Identify the blood parasite species.
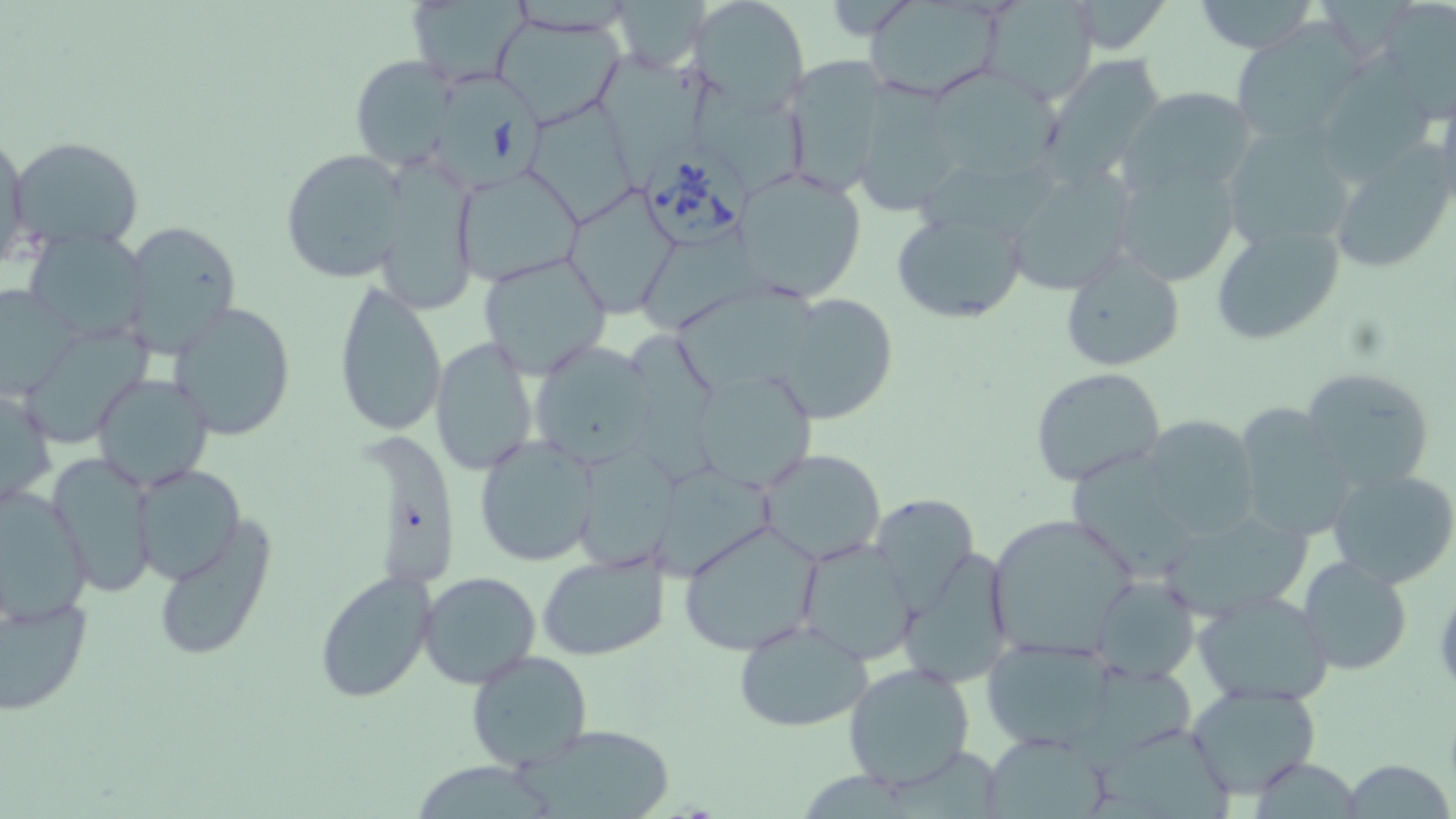

Babesia divergens.

Summary:
  - Coordinate format: approximate bounding boxes as named x1/y1/x2/y2 corners in pixels
  - Babesia divergens-infected red blood cell locations: (x1=435, y1=73, x2=552, y2=195), (x1=640, y1=151, x2=749, y2=247)
  - Uninfected red blood cell locations: (x1=612, y1=0, x2=708, y2=72), (x1=687, y1=0, x2=808, y2=114), (x1=980, y1=0, x2=1097, y2=106), (x1=1190, y1=0, x2=1322, y2=54), (x1=405, y1=1, x2=528, y2=85), (x1=861, y1=1, x2=1006, y2=100), (x1=1064, y1=2, x2=1174, y2=54), (x1=1376, y1=3, x2=1454, y2=115), (x1=493, y1=13, x2=625, y2=127), (x1=1231, y1=24, x2=1364, y2=149), (x1=588, y1=51, x2=716, y2=185), (x1=1040, y1=54, x2=1170, y2=179), (x1=350, y1=55, x2=467, y2=172), (x1=782, y1=56, x2=891, y2=194), (x1=928, y1=71, x2=1062, y2=180), (x1=693, y1=81, x2=818, y2=197), (x1=852, y1=84, x2=965, y2=216), (x1=1121, y1=86, x2=1257, y2=196), (x1=534, y1=104, x2=643, y2=228), (x1=1220, y1=124, x2=1360, y2=256), (x1=0, y1=134, x2=29, y2=268), (x1=8, y1=136, x2=146, y2=254), (x1=1327, y1=147, x2=1456, y2=275), (x1=282, y1=148, x2=410, y2=285), (x1=1110, y1=155, x2=1246, y2=287), (x1=371, y1=162, x2=481, y2=318), (x1=1004, y1=163, x2=1139, y2=296), (x1=453, y1=166, x2=585, y2=285), (x1=737, y1=167, x2=868, y2=302), (x1=562, y1=185, x2=682, y2=317), (x1=889, y1=207, x2=1029, y2=324), (x1=118, y1=218, x2=244, y2=358), (x1=1211, y1=218, x2=1347, y2=345), (x1=23, y1=229, x2=152, y2=343), (x1=1058, y1=248, x2=1186, y2=372), (x1=476, y1=252, x2=613, y2=377), (x1=332, y1=282, x2=448, y2=437), (x1=0, y1=285, x2=79, y2=399), (x1=770, y1=292, x2=899, y2=425), (x1=679, y1=293, x2=839, y2=400), (x1=169, y1=300, x2=297, y2=442), (x1=30, y1=317, x2=158, y2=440), (x1=429, y1=338, x2=538, y2=476), (x1=526, y1=339, x2=658, y2=468), (x1=1298, y1=364, x2=1436, y2=493), (x1=690, y1=366, x2=820, y2=493), (x1=1028, y1=366, x2=1167, y2=486), (x1=91, y1=372, x2=215, y2=491), (x1=0, y1=383, x2=55, y2=514), (x1=1231, y1=404, x2=1356, y2=542), (x1=1139, y1=414, x2=1261, y2=538), (x1=474, y1=435, x2=599, y2=566), (x1=757, y1=448, x2=888, y2=566), (x1=569, y1=449, x2=687, y2=576), (x1=48, y1=454, x2=158, y2=597), (x1=1068, y1=458, x2=1200, y2=576), (x1=133, y1=464, x2=246, y2=585), (x1=1326, y1=467, x2=1456, y2=589), (x1=651, y1=468, x2=782, y2=582), (x1=0, y1=485, x2=92, y2=626), (x1=870, y1=493, x2=978, y2=600), (x1=1155, y1=508, x2=1313, y2=622), (x1=989, y1=515, x2=1142, y2=658), (x1=153, y1=518, x2=275, y2=662), (x1=678, y1=520, x2=824, y2=658), (x1=794, y1=539, x2=920, y2=665), (x1=536, y1=548, x2=671, y2=662), (x1=898, y1=549, x2=1016, y2=687), (x1=1298, y1=556, x2=1412, y2=675), (x1=314, y1=570, x2=438, y2=701), (x1=419, y1=572, x2=542, y2=690), (x1=1090, y1=575, x2=1200, y2=684), (x1=1193, y1=590, x2=1333, y2=708), (x1=0, y1=595, x2=92, y2=715), (x1=731, y1=618, x2=877, y2=733), (x1=981, y1=634, x2=1117, y2=749), (x1=466, y1=649, x2=595, y2=772), (x1=842, y1=662, x2=975, y2=789), (x1=1184, y1=682, x2=1323, y2=800), (x1=1092, y1=723, x2=1247, y2=816), (x1=516, y1=725, x2=680, y2=819), (x1=979, y1=731, x2=1110, y2=818), (x1=1339, y1=760, x2=1455, y2=818)
  - Image size: 1456×819 pixels
  - Modality: light microscopy
  - Preparation: thin blood smear
  - Field of view: single
  - Magnification: 1000x
  - Stain: May-Grünwald-Giemsa